Locate every malaria parasite.
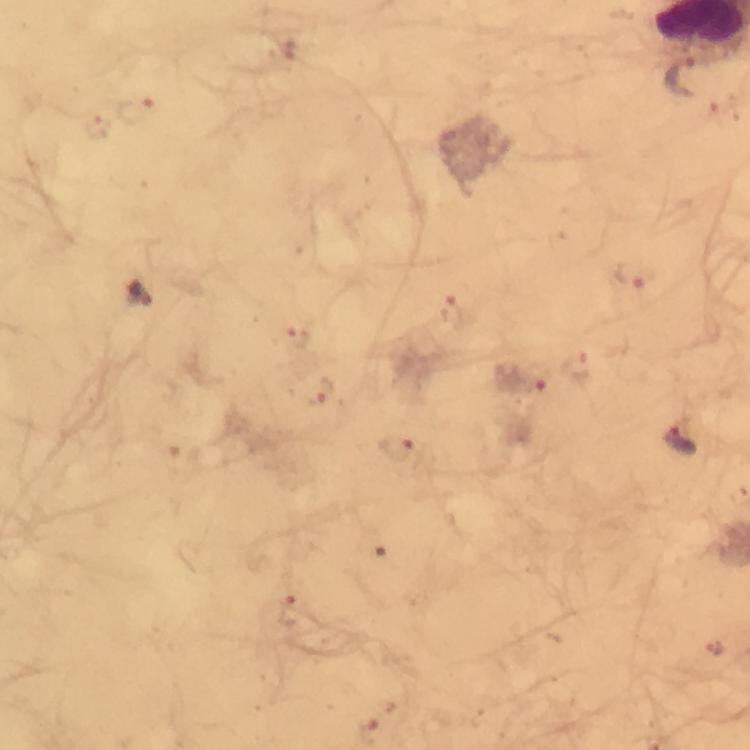
Approximate centers as (x, y) in pixels.
Malaria parasites: (683, 73), (138, 109), (633, 274), (144, 296), (453, 313), (298, 334), (522, 389), (322, 390), (681, 440), (397, 446), (290, 613), (716, 648).

magnification: 100x
cropped_from: one field of view
capture: smartphone photograph through a microscope
stain: Giemsa
image_size: 750×750 pixels
preparation: thick blood smear
immersion_oil: used
context: from a malaria diagnostic workup